Report the malaria status of this cell.
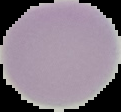
Uninfected.

image type = cell region segmented out of the field of view; surrounding area masked to black
preparation = thin blood smear
image size = 121×112 pixels